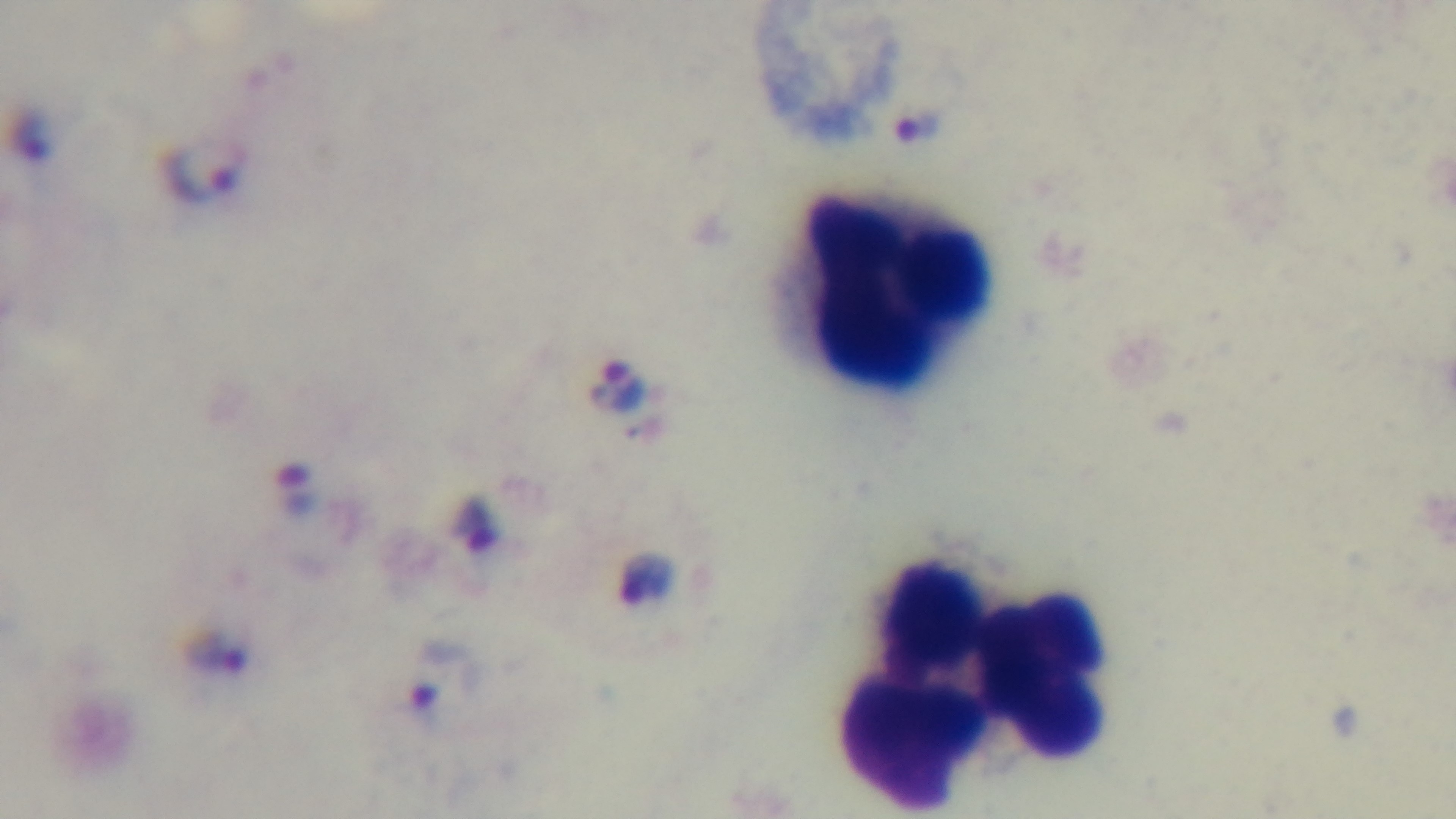

Single field of view. Malaria status: infected. Giemsa stain. Mounted 4K digital camera. Light microscopy. Preparation: thick. Oil-immersion objective, 100x.